Locate every Plasmodium parasite by life-cycle stage, and every leukocyte.
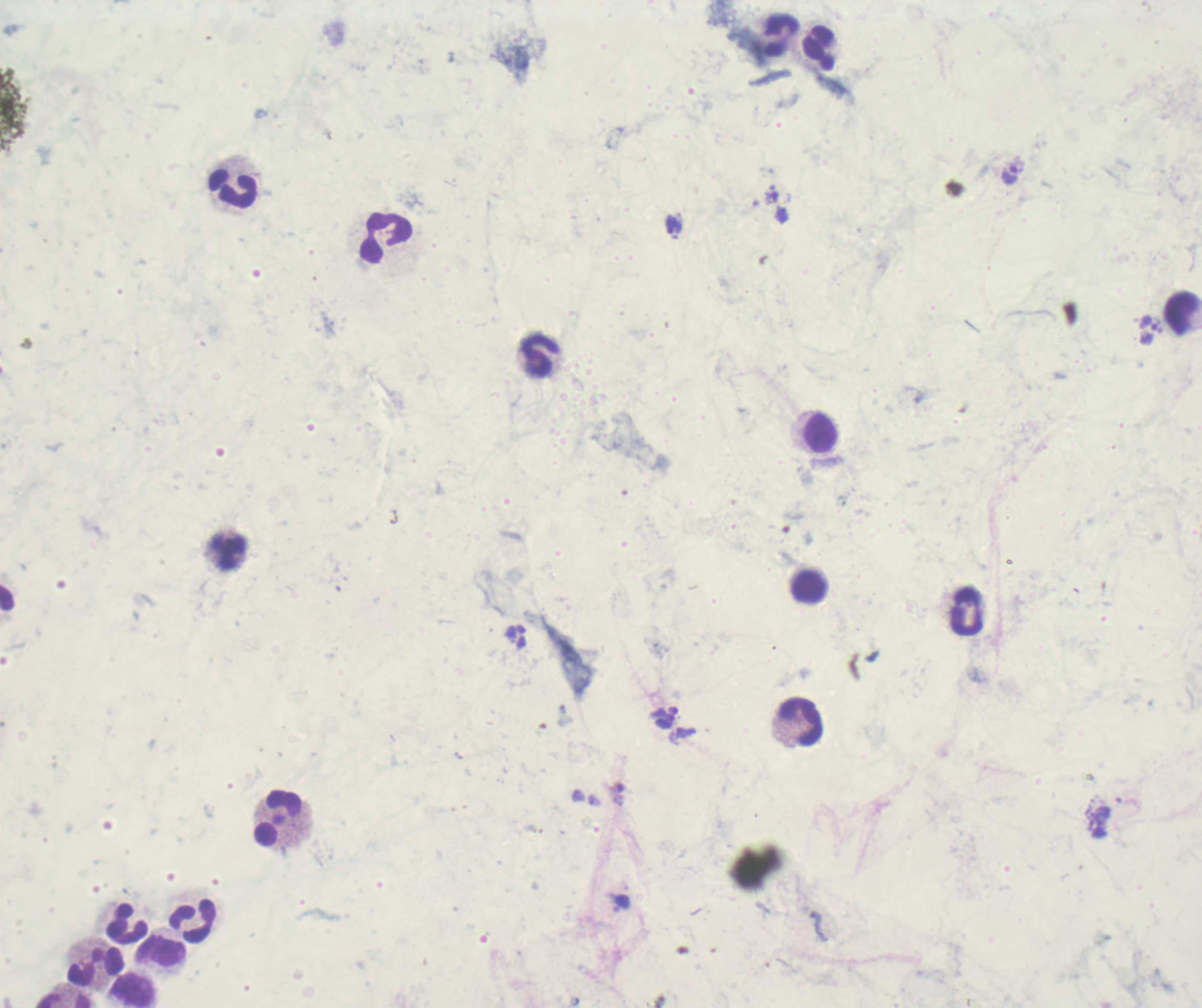
Approximate object centers, in pixels from the top-left corner.
Trophozoites: (x=1010, y=173), (x=672, y=223), (x=1153, y=325).
No schizont or gametocyte forms observed.
Leukocytes: (x=781, y=35), (x=820, y=48), (x=233, y=189), (x=386, y=238), (x=1182, y=313), (x=540, y=355), (x=820, y=434), (x=224, y=549), (x=809, y=587), (x=966, y=609), (x=801, y=723), (x=278, y=819), (x=191, y=920), (x=125, y=924), (x=161, y=950), (x=94, y=964), (x=132, y=991), (x=63, y=1000).

Summary:
  - Background quality: unsatisfactory
  - Magnification: 100x
  - Field of view: one from this slide
  - Image size: 1202×1008 pixels
  - Preparation: thick blood smear
  - Coloration quality: bad
  - Stain: Romanowsky
  - Context: previously used in a real diagnosis